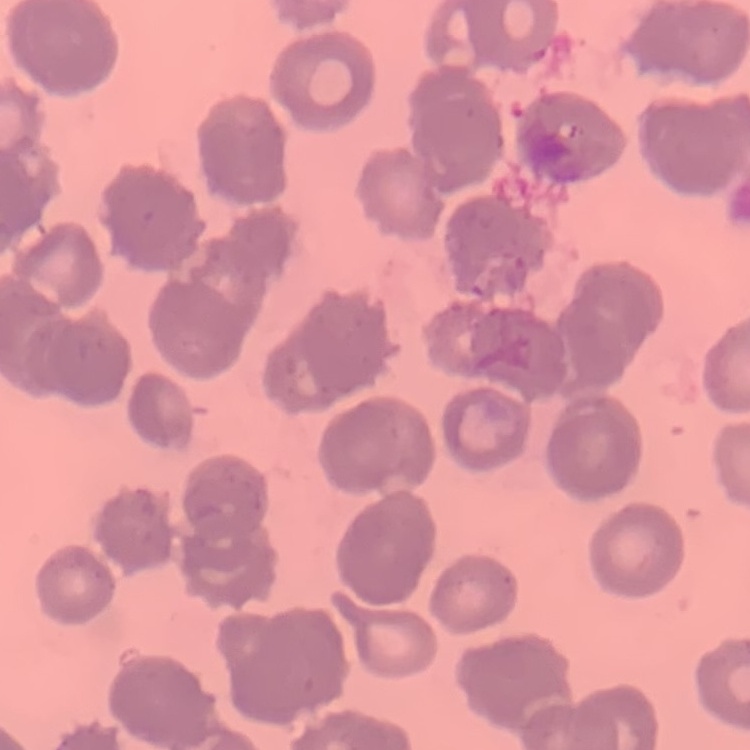
The erythrocytes exhibit rouleaux formation. Thin peripheral smear. Field's or Giemsa stain. One tile cut from a larger photomicrograph.